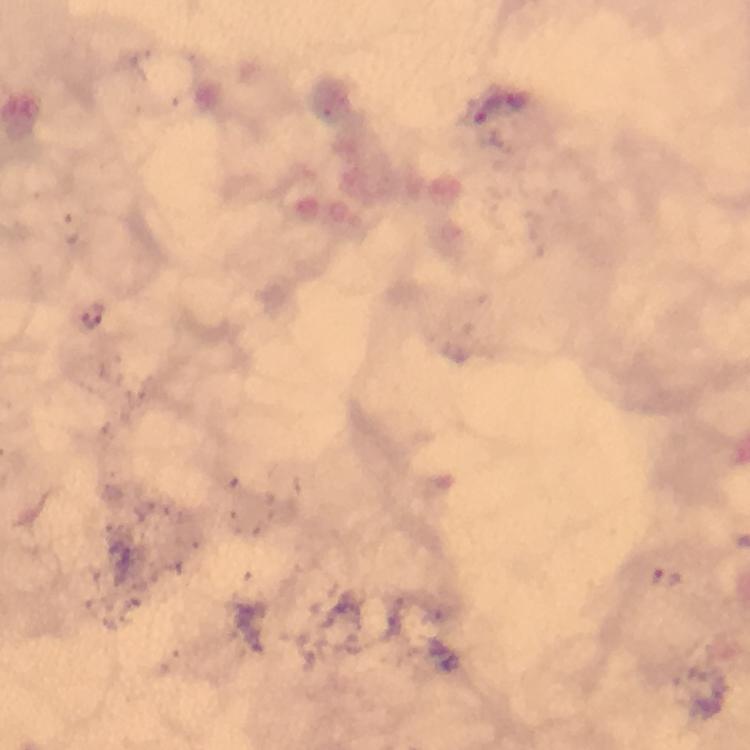
image size = 750×750 pixels
capture = smartphone camera through the microscope
cropped from = one field of view
Plasmodium parasite locations = approximate centers as (x, y) in pixels: (519, 104), (491, 106), (71, 230), (667, 577)
preparation = thick blood film
stain = Giemsa
context = from a malaria diagnostic workup
immersion oil = applied
magnification = 100x